Locate every blood parasite and identify its species.
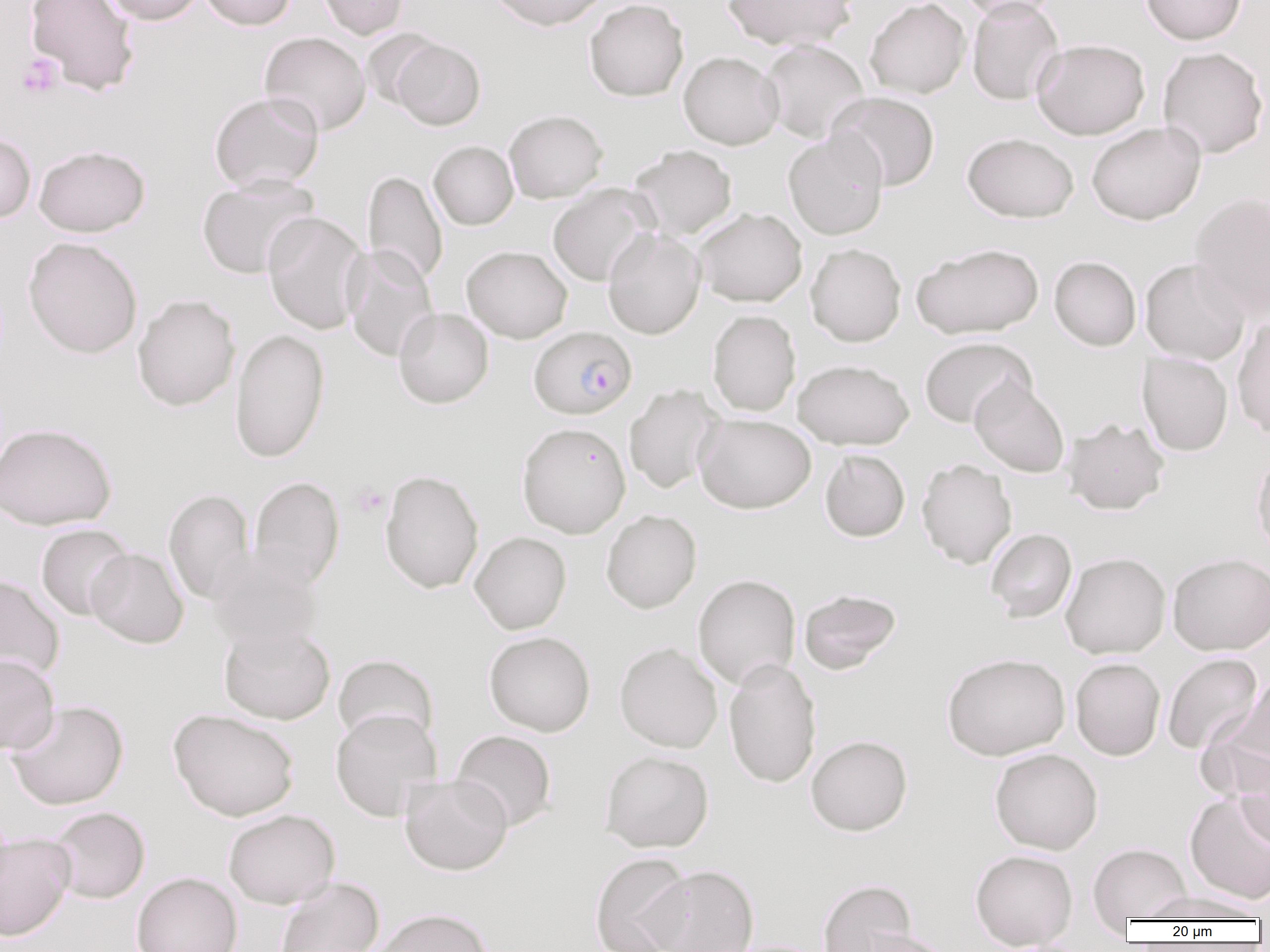
Approximate bounding boxes as [x1, y1, x2, y2] in pixels.
Plasmodium falciparum-infected red blood cells: [529, 326, 637, 419].
No Plasmodium ovale, Plasmodium malariae, Plasmodium vivax, Babesia divergens, or Trypanosoma brucei observed.

{
  "slide_level_diagnosis": "Plasmodium falciparum",
  "uninfected_red_blood_cell_locations": "approximate bounding boxes as [x1, y1, x2, y2] in pixels: [24, 0, 141, 97], [102, 0, 205, 25], [198, 0, 296, 30], [317, 0, 409, 39], [487, 0, 608, 31], [584, 0, 689, 102], [722, 0, 856, 50], [865, 0, 970, 98], [955, 0, 1064, 21], [967, 0, 1065, 106], [1140, 0, 1246, 45], [362, 29, 444, 110], [259, 31, 371, 136], [391, 38, 486, 130], [1032, 38, 1150, 139], [759, 39, 870, 143], [1157, 46, 1269, 159], [678, 51, 784, 150], [209, 91, 324, 193], [826, 91, 940, 191], [504, 109, 608, 203], [1086, 121, 1206, 225], [0, 131, 36, 224], [783, 131, 889, 240], [962, 132, 1079, 223], [429, 141, 518, 230], [34, 145, 150, 237], [627, 145, 738, 241], [363, 170, 448, 287], [196, 173, 320, 280], [547, 184, 656, 286], [1189, 192, 1270, 321], [693, 207, 807, 307], [263, 212, 368, 335], [603, 228, 705, 339], [23, 237, 143, 359], [805, 243, 906, 346], [911, 243, 1044, 339], [461, 245, 573, 344], [342, 246, 439, 363], [1049, 256, 1141, 351], [1140, 258, 1250, 365], [132, 294, 240, 411], [393, 307, 493, 408], [707, 309, 801, 416], [1232, 316, 1270, 441], [230, 328, 329, 464], [919, 336, 1035, 428], [1137, 352, 1233, 456], [793, 359, 914, 450], [970, 377, 1069, 477], [624, 384, 725, 494], [694, 413, 816, 514], [1062, 417, 1170, 515], [517, 422, 631, 538], [0, 423, 116, 530], [820, 449, 910, 542], [1251, 449, 1270, 561], [917, 458, 1017, 569], [379, 469, 485, 594], [249, 476, 344, 589], [163, 489, 256, 604], [601, 509, 702, 613], [35, 524, 135, 621], [985, 528, 1077, 623], [469, 531, 571, 634], [208, 546, 323, 654], [86, 548, 188, 648], [1060, 551, 1171, 659], [1167, 553, 1270, 655], [0, 574, 65, 684], [693, 574, 801, 689], [798, 588, 902, 675], [219, 623, 335, 725], [484, 631, 596, 736], [615, 642, 723, 753], [941, 652, 1070, 760], [1162, 653, 1262, 755], [0, 654, 60, 754], [333, 654, 439, 749], [1070, 657, 1165, 760], [723, 658, 822, 789], [1225, 678, 1269, 774], [5, 699, 129, 810], [168, 708, 300, 821], [330, 708, 443, 820], [451, 729, 557, 832], [806, 734, 913, 836], [989, 748, 1103, 855], [600, 750, 714, 852], [1234, 757, 1270, 852], [399, 774, 512, 876], [1184, 793, 1270, 905], [48, 807, 150, 903], [223, 809, 341, 909], [0, 832, 76, 940], [1088, 843, 1192, 923], [970, 849, 1078, 951], [589, 851, 693, 952], [645, 864, 760, 952], [132, 872, 242, 952], [274, 877, 385, 952], [817, 879, 918, 952], [1141, 890, 1261, 921], [372, 907, 494, 952], [851, 928, 956, 952], [717, 939, 830, 952]",
  "field_of_view": "one of a larger specimen",
  "image_size": "1270×952 pixels",
  "modality": "optical microscopy",
  "magnification": "1000x",
  "preparation": "thin blood smear",
  "platelet_locations": "approximate bounding boxes as [x1, y1, x2, y2] in pixels: [15, 53, 64, 99], [349, 483, 388, 519]"
}